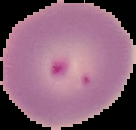

Result: malaria parasites identified. Cell region segmented out of the field of view; the surrounding area is masked to black. From a thin blood smear. Image is 136×130 pixels.